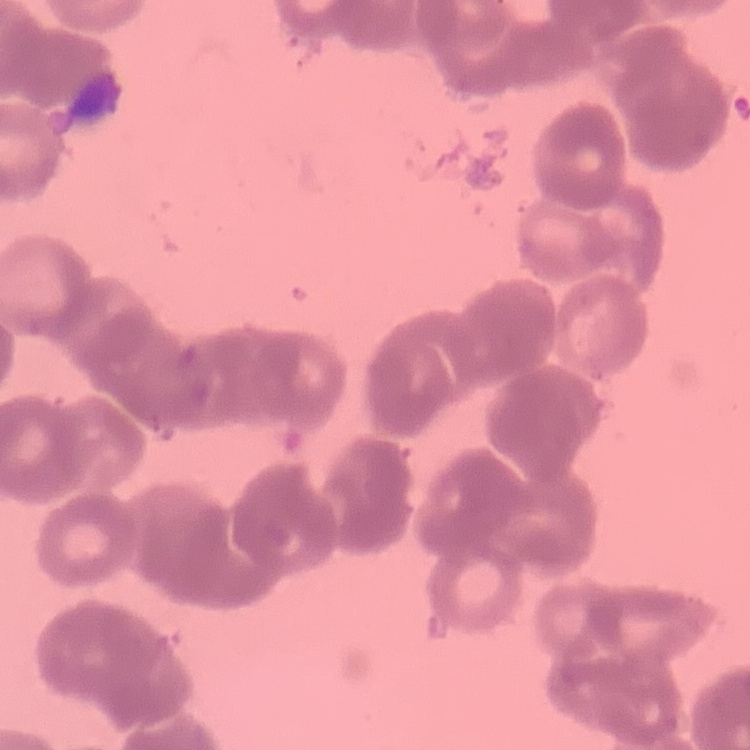
The red blood cells show rouleaux formation. Square crop of a larger photomicrograph. Field's or Giemsa stain. Thin blood film.